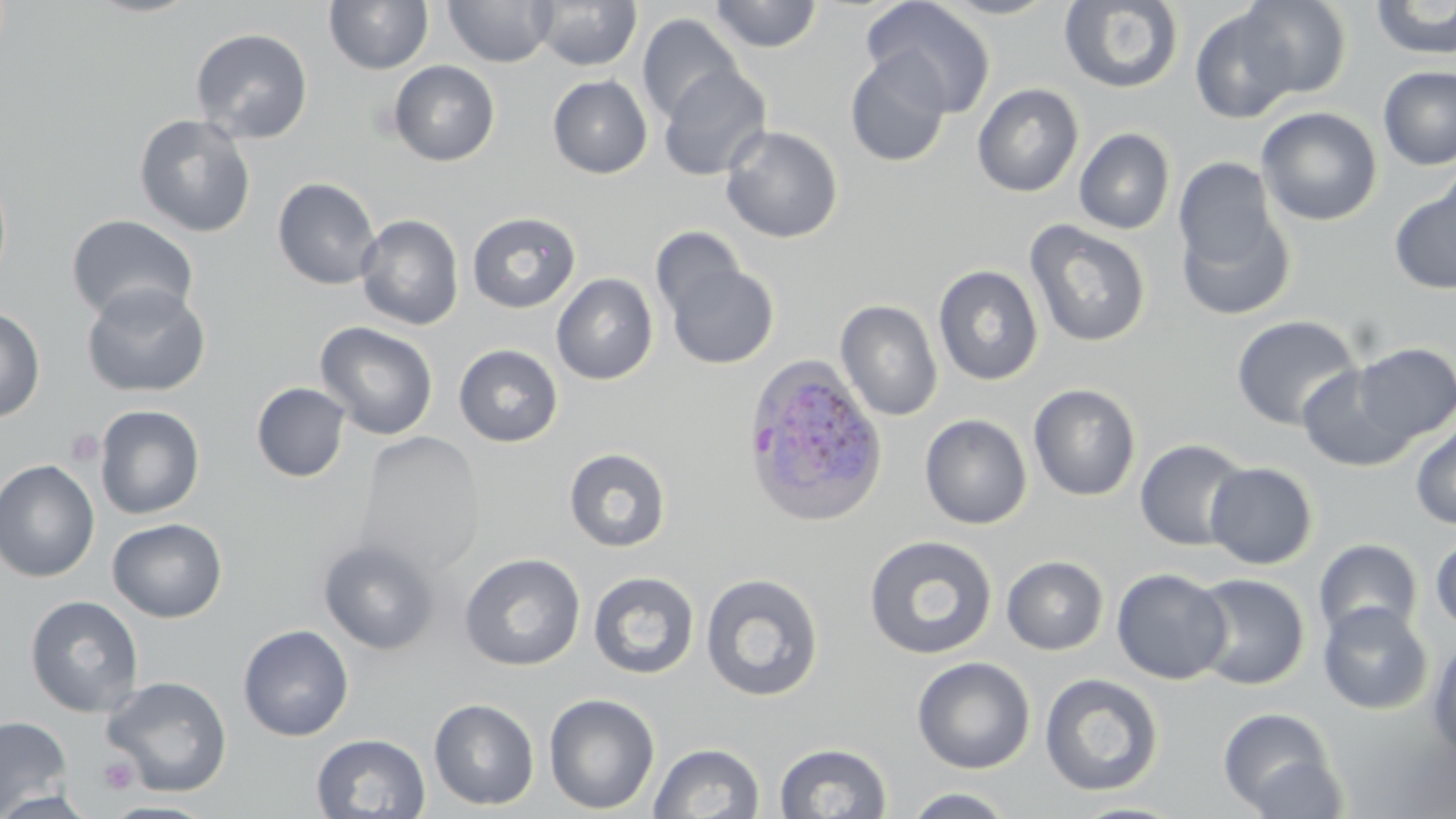

Summary:
  - Coordinate format: approximate bounding boxes as (x1,y1)-(x2,y2) corner pairs in pixels
  - Uninfected red blood cell locations: (83,0)-(205,18), (324,0)-(434,74), (531,0)-(642,71), (709,0)-(823,52), (933,0)-(1063,20), (1059,0)-(1184,94), (1235,0)-(1352,99), (1370,0)-(1456,59), (443,1)-(556,68), (861,1)-(996,117), (1189,8)-(1301,124), (637,13)-(744,124), (190,27)-(313,143), (844,51)-(952,168), (388,60)-(500,166), (658,65)-(772,181), (1378,66)-(1456,171), (547,75)-(652,179), (972,82)-(1084,197), (1256,106)-(1382,226), (133,113)-(256,238), (720,124)-(843,244), (1074,128)-(1175,235), (1172,158)-(1295,320), (272,177)-(381,290), (1389,179)-(1456,295), (467,211)-(581,313), (66,214)-(199,325), (355,214)-(465,331), (1024,220)-(1151,348), (650,227)-(748,322), (662,259)-(780,369), (933,264)-(1043,385), (551,273)-(659,385), (81,282)-(211,398), (835,299)-(942,421), (0,304)-(46,423), (1231,314)-(1362,431), (314,321)-(439,441), (1350,342)-(1455,444), (453,344)-(563,447), (1296,361)-(1420,472), (251,382)-(351,482), (1028,383)-(1142,501), (94,404)-(205,519), (920,413)-(1032,529), (1410,420)-(1456,530), (355,430)-(485,578), (1135,439)-(1250,551), (564,447)-(671,552), (0,459)-(101,582), (1205,461)-(1318,569), (107,517)-(227,622), (863,534)-(999,660), (1430,534)-(1456,634), (318,538)-(441,655), (1313,538)-(1423,641), (459,553)-(586,671), (1001,555)-(1109,655), (1111,568)-(1232,685), (587,570)-(700,679), (699,571)-(825,702), (1189,573)-(1310,689), (24,595)-(144,718), (1317,602)-(1433,715), (238,624)-(354,741), (1426,638)-(1456,761), (912,656)-(1035,774), (1040,673)-(1164,796), (102,676)-(232,797), (544,693)-(661,814), (429,698)-(540,810), (1218,706)-(1341,817), (0,716)-(73,816), (310,733)-(431,818), (649,742)-(765,819), (774,742)-(892,819), (900,786)-(1019,818), (0,789)-(100,819), (100,800)-(219,818), (1067,800)-(1191,819)
  - Platelet locations: (64,427)-(105,467), (98,757)-(139,795)
  - Plasmodium ovale-infected red blood cell locations: (741,353)-(888,526)
  - Slide-level diagnosis: Plasmodium ovale
  - Image size: 1456×819 pixels
  - Stain: May-Grünwald-Giemsa
  - Modality: optical microscopy
  - Magnification: 1000x
  - Preparation: thin blood film
  - Field of view: single